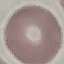
Malaria status: uninfected. Thin blood smear. Cell patch, automatically extracted from a larger field of view and resized to 64 × 64 pixels. Giemsa stain. Acquired by smartphone through the microscope eyepiece.